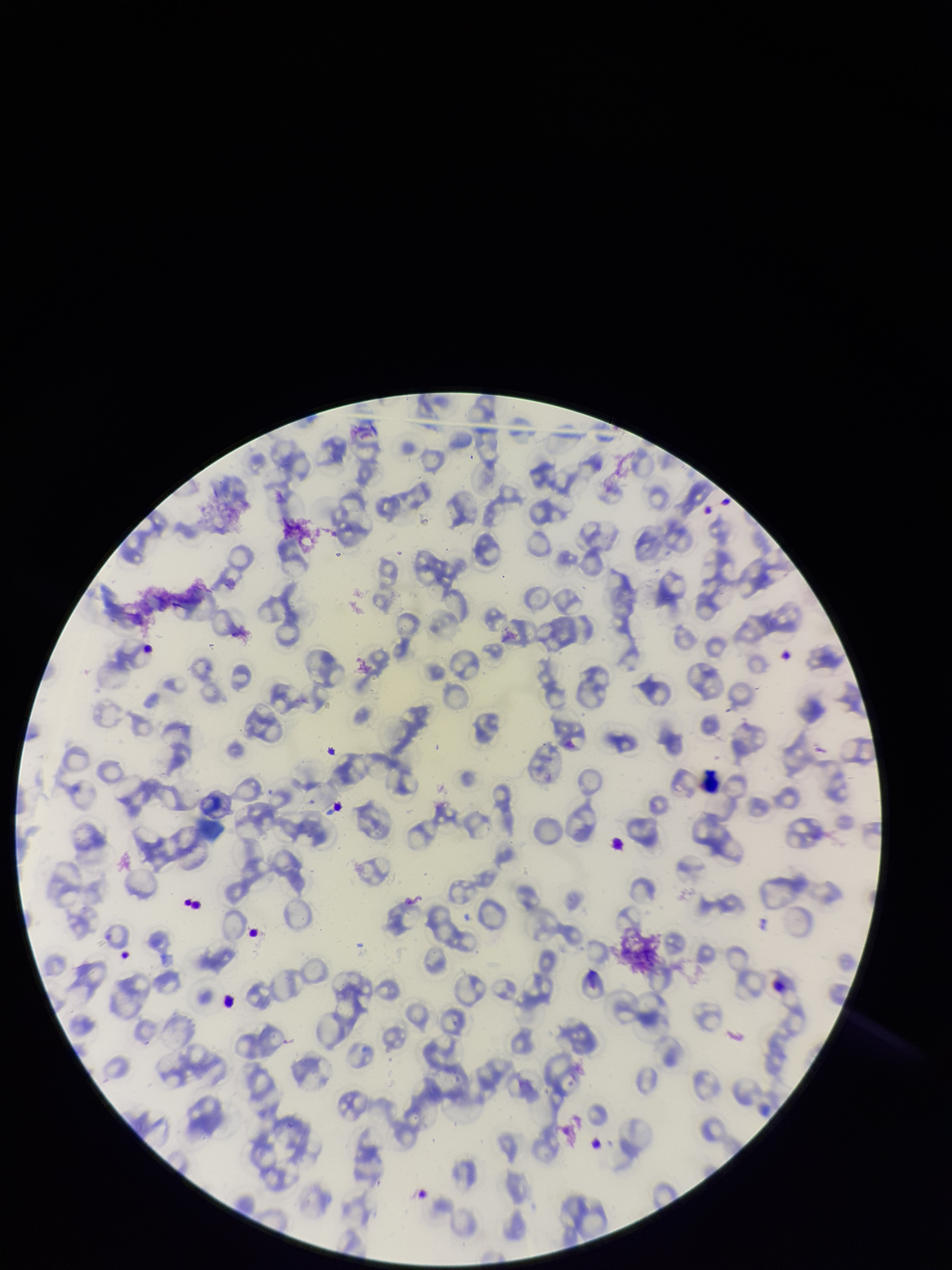

Summary:
  - Patient malaria status: infected
  - Stain: Giemsa
  - Parasitized red blood cell count: 0
  - Red blood cell count: 123
  - Field of view: single
  - Parasitized red blood cells: none identified
  - Species reported for this patient: Plasmodium falciparum
  - Preparation: thin
  - Image size: 952×1270 pixels
  - Capture: smartphone photograph through the microscope eyepiece